Describe the morphology of the red blood cells.
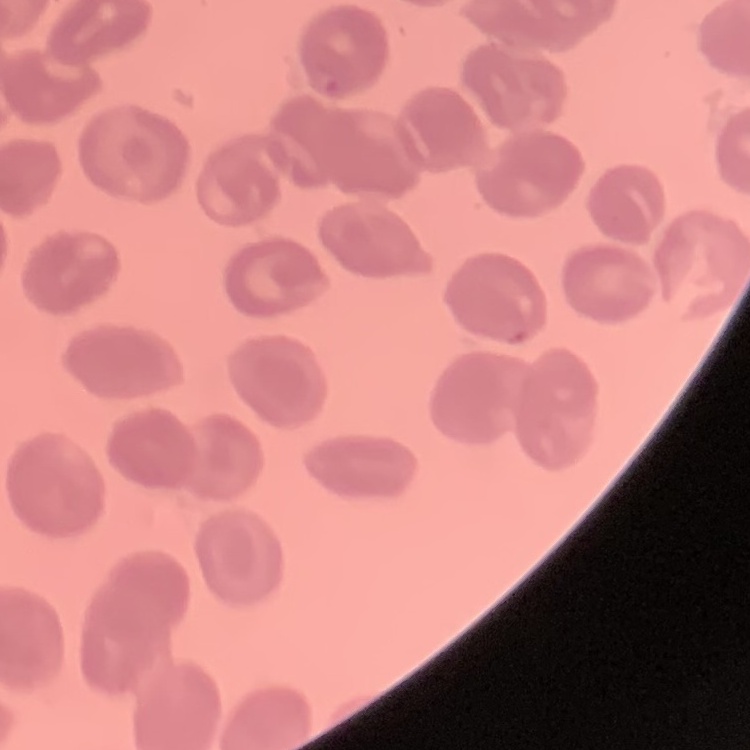
No rouleaux formation.

One tile cut from a larger photomicrograph. Thin blood smear. Field's or Giemsa stain.